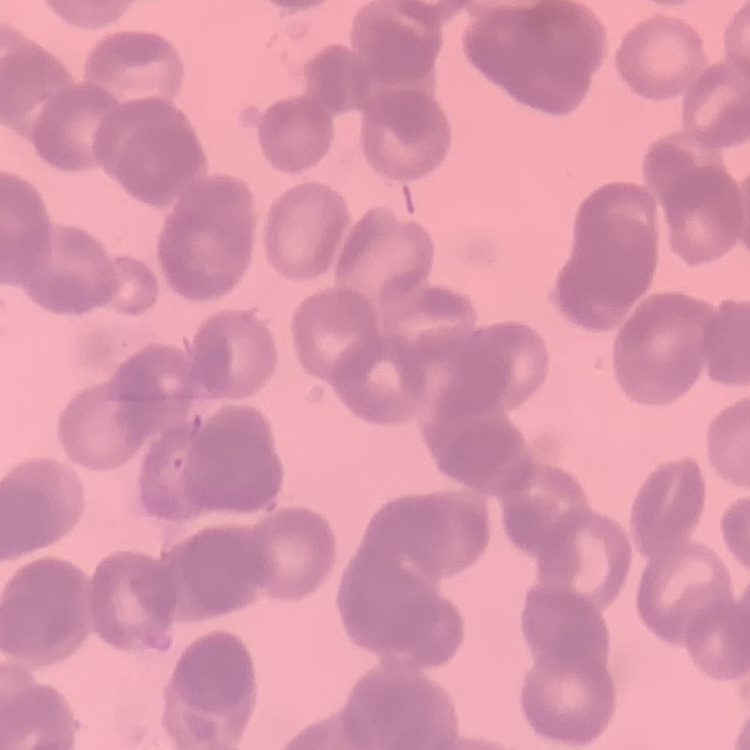

The red blood cells exhibit rouleaux formation. Square crop of a larger photomicrograph. Stained with either Field's or Giemsa. Thin peripheral smear.